Draw a bounding box around every parasitised red blood cell, every trophozoite, every gametocyte, every leukocyte, and every artifact (platelet-like body, stain precipitate, or debris).
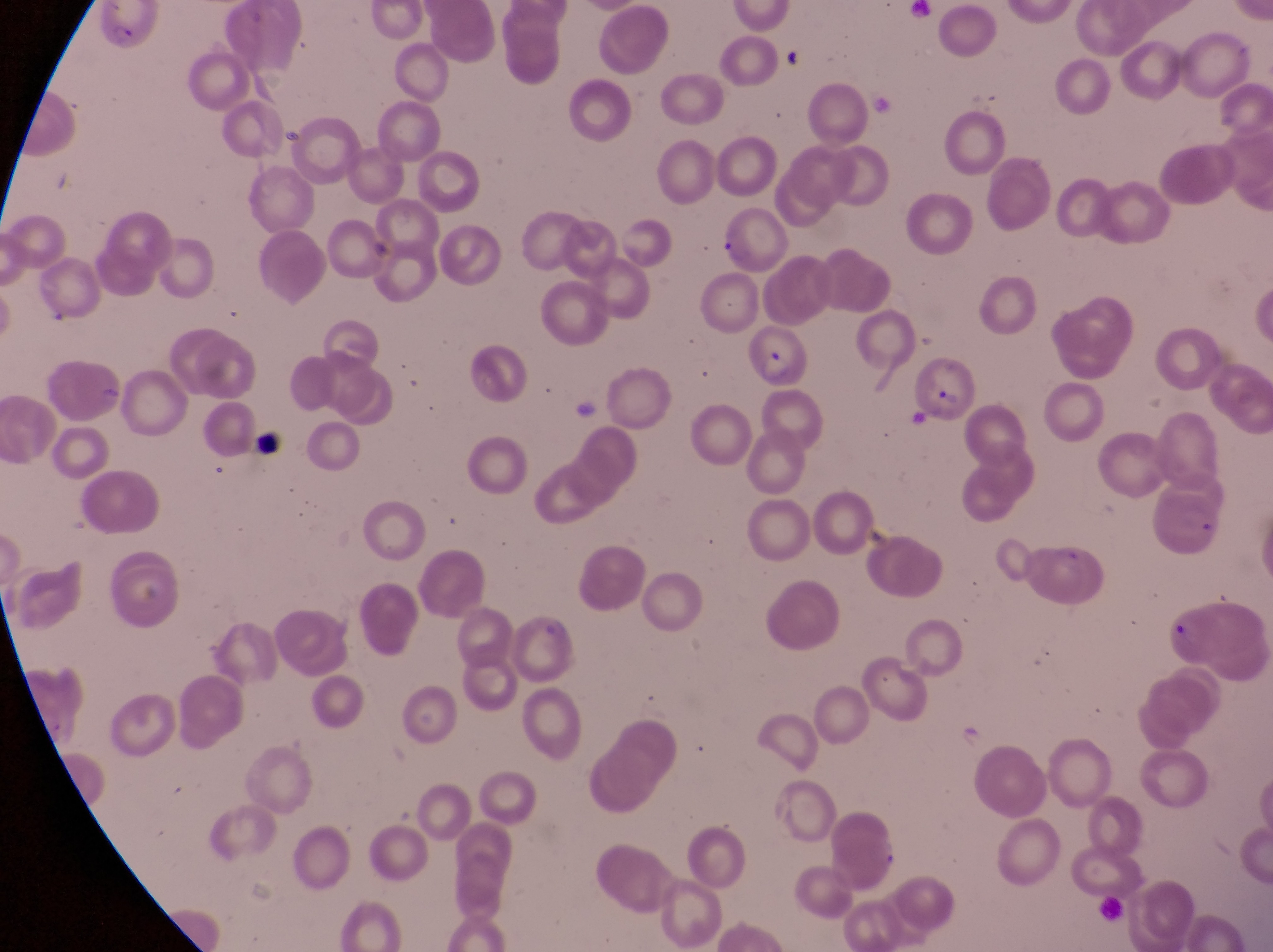
Approximate bounding boxes as left top right bottom in pixels.
Parasitised red blood cells: 711 204 789 269; 756 329 811 387; 909 350 979 424; 1165 609 1239 672.
No leukocytes observed.
Artifacts (platelet-like body, stain precipitate, or debris): 774 43 814 75; 250 427 283 457.

Summary:
  - Preparation: thin blood smear
  - Capture: smartphone photograph through the eyepiece of an Olympus CX-23 microscope
  - Country: Uganda
  - Magnification: 1000x
  - Field of view: single
  - Image size: 1273×952 pixels